Classify this cell by malaria status.
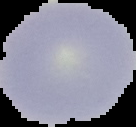

Uninfected.

{
  "image_size": "136×127 pixels",
  "image_type": "segmented cell region on a black background",
  "preparation": "thin blood film"
}